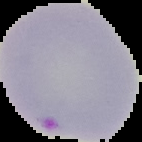

image size = 142×142 pixels
preparation = thin blood film
image type = cell region segmented out of the field of view; surrounding area masked to black
malaria status = parasitized